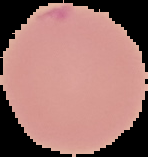 From a thin blood smear. Image is 148×157 pixels. The area outside the segmented cell region is set to black. Result: negative for Plasmodium parasites.